Identify the parasite.
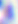

This is Toxoplasma gondii.

Captured at 400x magnification. Photomicrograph.